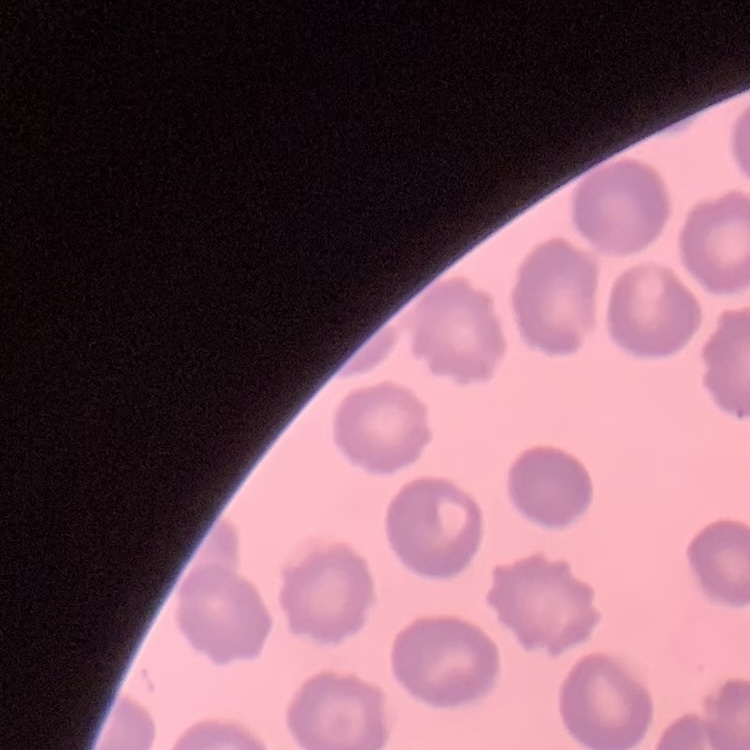
red_blood_cell_morphology: no rouleaux formation
stain: Field's or Giemsa
image_type: one tile cut from a larger photomicrograph
preparation: thin blood smear